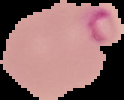
Result: Plasmodium parasites detected. Image is 124×100 pixels. From a thin blood smear. The area outside the segmented cell region is set to black.